Name the cell type shown.
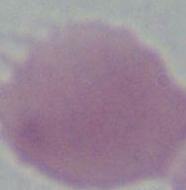
An erythrocyte.

Photomicrograph. 1000x magnification.